Point out each malaria parasite.
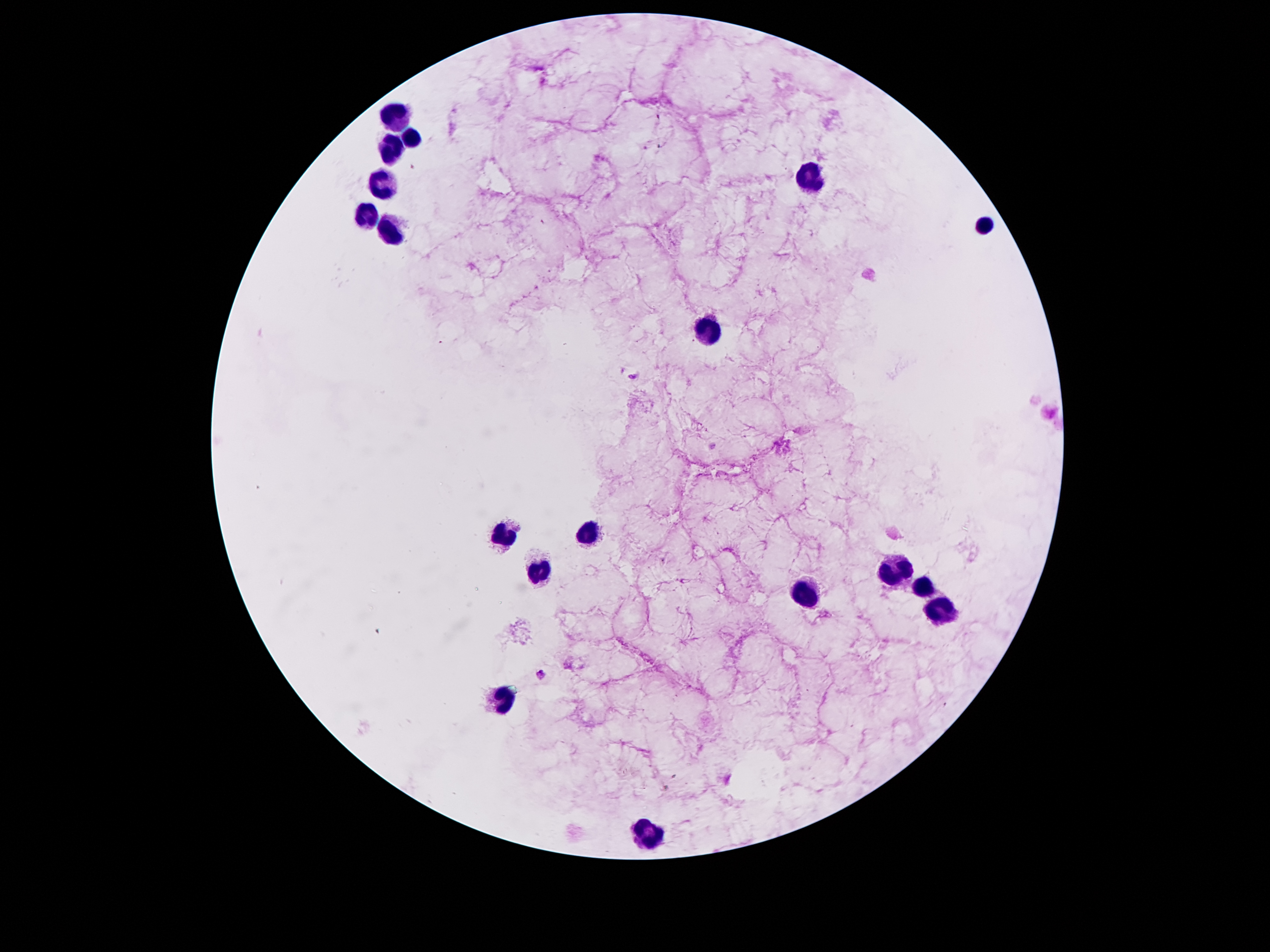
Approximate object centers, in pixels from the top-left corner.
Malaria parasites: (x=634, y=376), (x=540, y=675).

Summary:
  - Leukocyte locations: (x=395, y=116), (x=411, y=138), (x=390, y=151), (x=810, y=180), (x=382, y=188), (x=367, y=216), (x=984, y=224), (x=391, y=228), (x=708, y=333), (x=583, y=532), (x=505, y=536), (x=894, y=571), (x=541, y=572), (x=920, y=588), (x=803, y=591), (x=940, y=611), (x=500, y=700), (x=650, y=838)
  - Magnification: 100x
  - Capture: smartphone through the microscope eyepiece
  - Field of view: one from this slide
  - Image size: 1270×952 pixels
  - Stain: Giemsa
  - Patient malaria status: infected with Plasmodium falciparum
  - Preparation: thick blood smear